Classify this cell by malaria status.
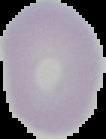

It is uninfected.

Image is 106×139 pixels. The area outside the segmented cell region is set to black. From a thin blood smear.